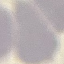

Summary:
  - Result: negative for malaria parasites
  - Stain: Giemsa
  - Image type: automatically extracted cell patch, resized to 64 × 64 pixels
  - Capture: smartphone through the microscope eyepiece
  - Preparation: thin blood film